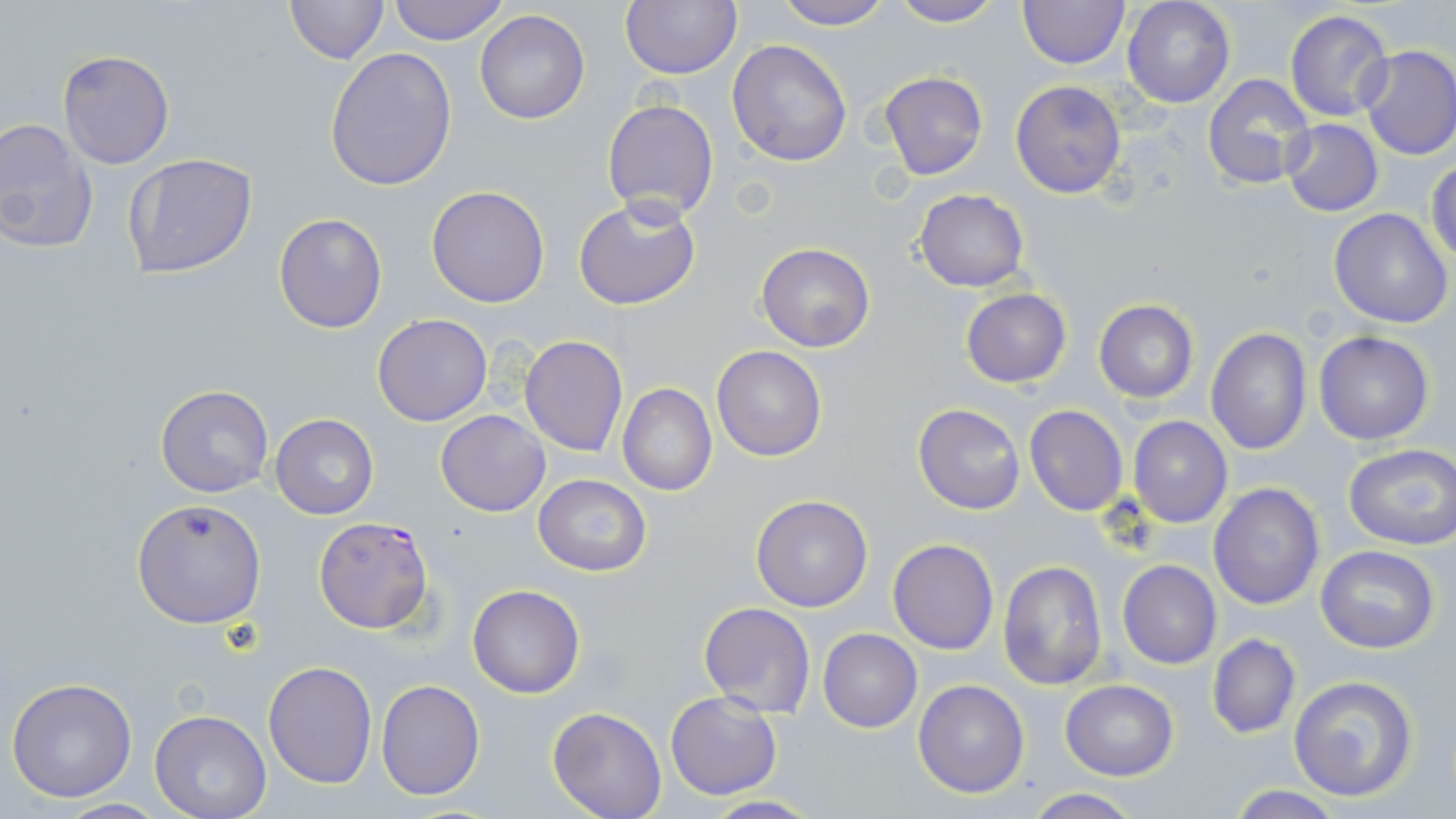
Summary:
  - Coordinate format: approximate bounding boxes as (x1, y1, x2, y2) in pixels
  - Plasmodium falciparum-infected red blood cell locations: (311, 516, 434, 635)
  - Uninfected red blood cell locations: (284, 0, 389, 64), (386, 0, 510, 45), (622, 0, 741, 79), (769, 0, 893, 29), (1016, 0, 1128, 69), (1122, 0, 1235, 108), (889, 1, 1006, 27), (1284, 10, 1395, 123), (475, 11, 590, 125), (728, 40, 853, 168), (1356, 45, 1456, 162), (325, 48, 457, 192), (57, 50, 175, 169), (877, 70, 989, 180), (1203, 72, 1316, 191), (1010, 80, 1128, 199), (601, 98, 721, 222), (0, 118, 97, 255), (1280, 119, 1384, 217), (122, 152, 259, 278), (1427, 159, 1456, 266), (426, 185, 550, 308), (912, 189, 1029, 292), (574, 196, 702, 312), (1330, 209, 1453, 330), (274, 212, 388, 333), (755, 243, 875, 351), (961, 289, 1071, 387), (1093, 299, 1199, 402), (372, 313, 493, 426), (1206, 328, 1312, 456), (1314, 331, 1435, 444), (519, 335, 630, 457), (711, 346, 827, 461), (618, 383, 717, 496), (154, 385, 274, 498), (914, 403, 1025, 515), (1023, 405, 1129, 517), (436, 409, 550, 517), (270, 413, 378, 520), (1127, 416, 1232, 528), (1344, 443, 1456, 550), (532, 474, 652, 575), (1208, 481, 1326, 612), (749, 493, 874, 611), (132, 498, 266, 628), (887, 537, 999, 654), (1315, 544, 1440, 653), (996, 559, 1108, 691), (1118, 561, 1221, 668), (466, 584, 586, 698), (698, 601, 816, 717), (819, 628, 922, 731), (1207, 634, 1301, 739), (263, 661, 378, 787), (1288, 674, 1420, 802), (6, 677, 137, 803), (376, 679, 486, 802), (913, 679, 1030, 800), (1060, 679, 1178, 781), (664, 692, 783, 800), (547, 707, 667, 819), (150, 710, 272, 819), (1222, 787, 1348, 818), (1023, 789, 1146, 819), (696, 796, 824, 817)
  - Slide-level diagnosis: Plasmodium falciparum
  - Modality: optical microscopy
  - Field of view: single
  - Preparation: thin blood film
  - Magnification: 1000x
  - Stain: May-Grünwald-Giemsa
  - Image size: 1456×819 pixels